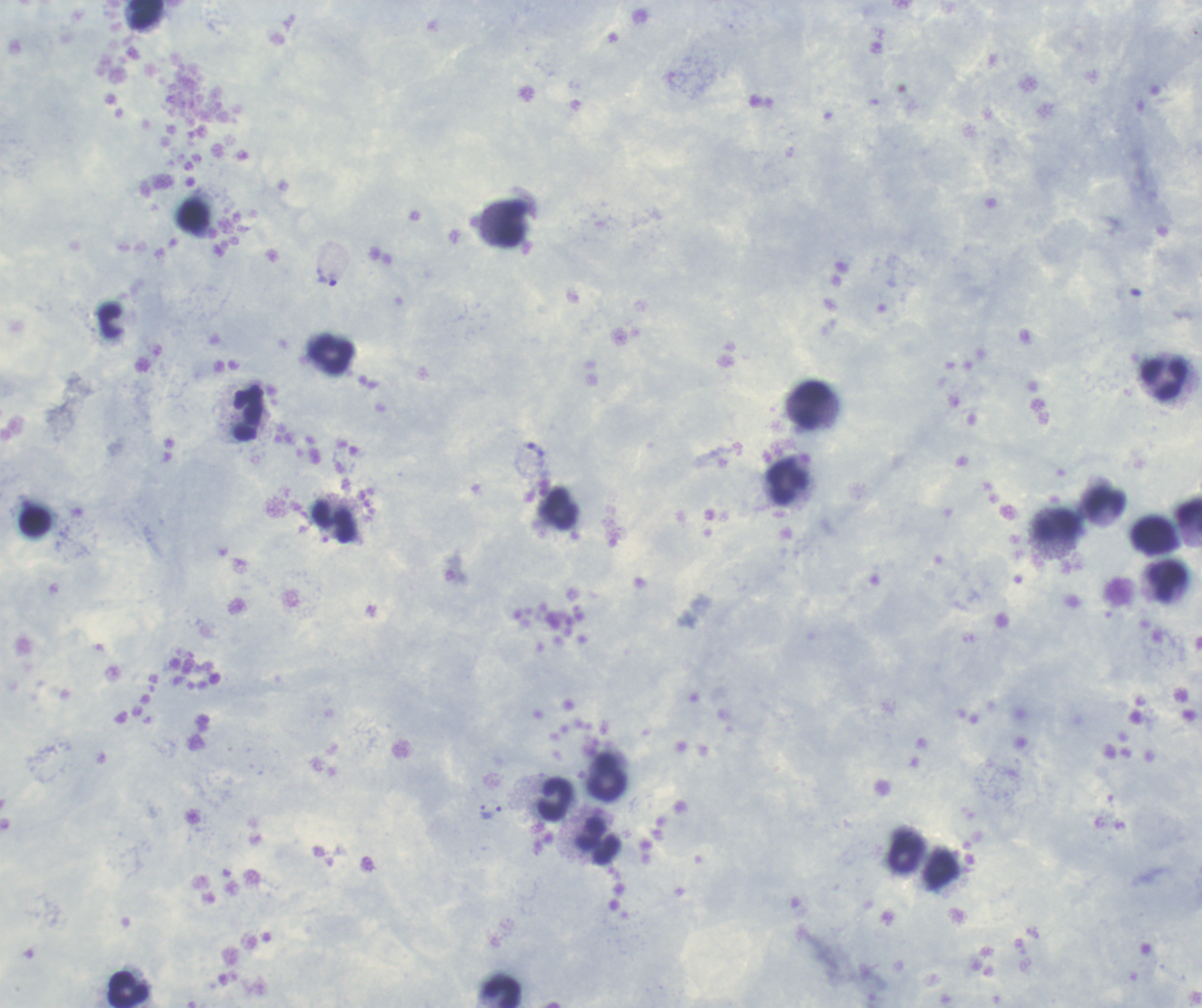

Coloration quality: good. Image is 1202×1008 pixels. Single field of view. Romanowsky stain. Thick blood smear.